Classify this cell by malaria status.
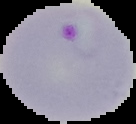
It is parasitized.

The area outside the segmented cell region is set to black. From a thin blood smear. Image is 136×124 pixels.